Report the malaria status of this cell.
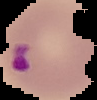
It is parasitized.

image type = cell region segmented out of the field of view; surrounding area masked to black
image size = 97×100 pixels
preparation = thin blood film